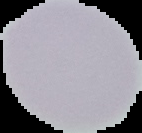

image_size: 142×133 pixels
image_type: cell region segmented out of the field of view; surrounding area masked to black
malaria_status: uninfected
preparation: thin blood smear